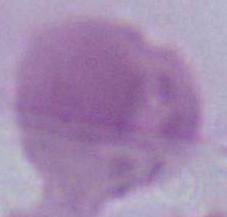

Summary:
  - Identification: red blood cell
  - Magnification: 1000x
  - Modality: photomicrograph